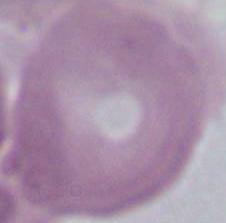 An erythrocyte is seen. Captured at 1000x magnification. Micrograph.